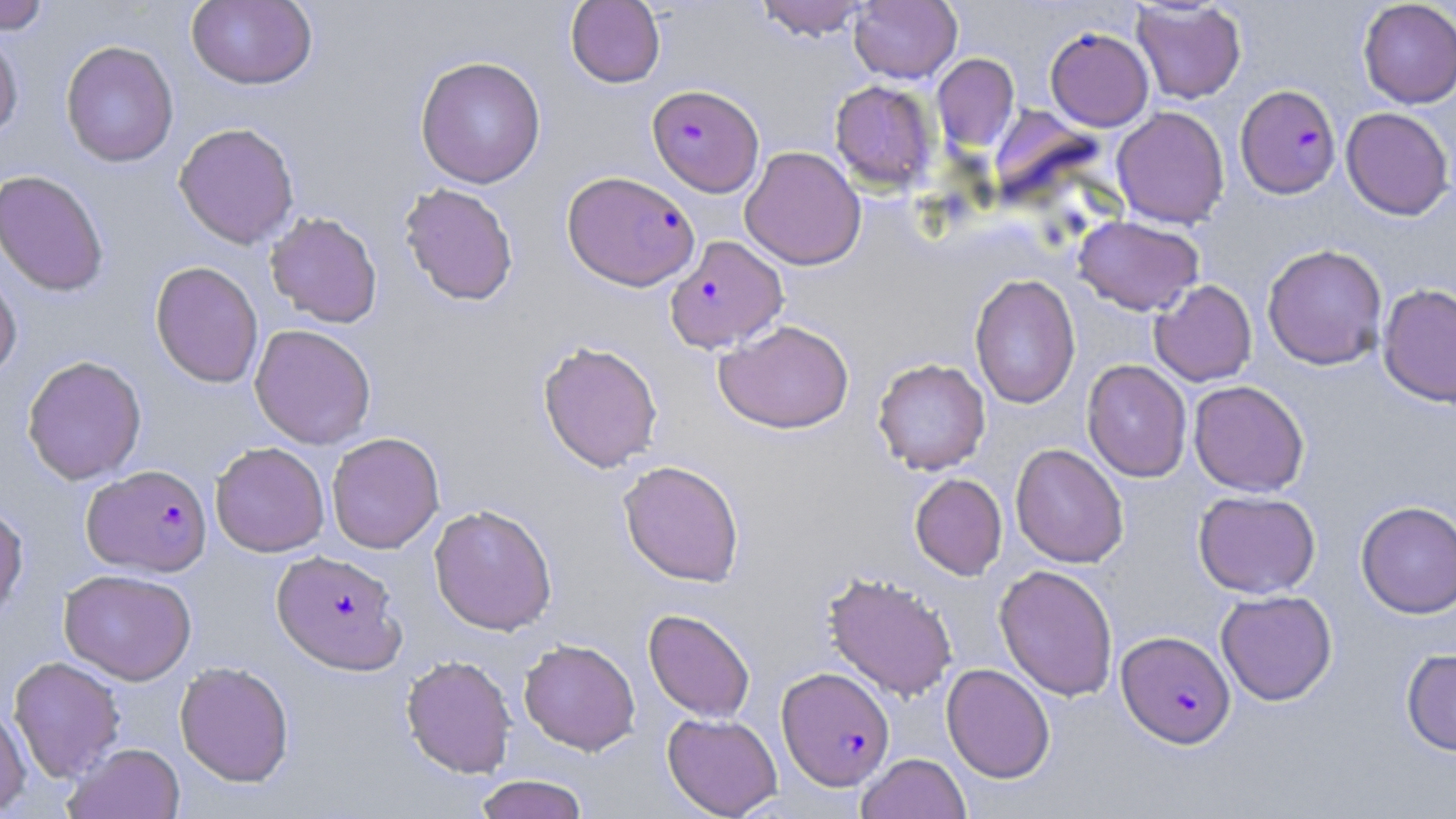
Summary:
  - Coordinate format: approximate bounding boxes as (x1, y1, x2, y2) in pixels
  - Plasmodium falciparum-infected red blood cell locations: (647, 84, 764, 197), (1236, 84, 1341, 199), (562, 170, 700, 291), (665, 235, 788, 354), (83, 464, 212, 577), (272, 550, 406, 675), (1117, 630, 1235, 748), (777, 666, 894, 790)
  - Uninfected red blood cell locations: (0, 0, 52, 33), (186, 0, 317, 90), (565, 0, 665, 87), (752, 0, 872, 40), (849, 0, 962, 83), (1131, 1, 1247, 104), (1358, 1, 1456, 108), (1045, 26, 1154, 131), (0, 27, 23, 144), (60, 40, 179, 167), (932, 53, 1020, 152), (415, 55, 546, 188), (829, 80, 938, 191), (991, 105, 1106, 212), (1111, 106, 1230, 229), (1341, 107, 1455, 220), (174, 122, 299, 249), (740, 146, 866, 270), (0, 169, 110, 296), (399, 182, 519, 306), (265, 211, 383, 328), (1073, 216, 1204, 315), (1262, 243, 1388, 370), (150, 261, 264, 388), (0, 264, 22, 382), (969, 273, 1081, 409), (1150, 280, 1257, 386), (1377, 283, 1456, 408), (714, 319, 854, 433), (250, 324, 376, 449), (538, 340, 664, 473), (22, 355, 147, 485), (872, 357, 991, 475), (1081, 360, 1192, 482), (1188, 380, 1310, 497), (326, 431, 445, 554), (210, 442, 329, 557), (1010, 443, 1129, 568), (618, 459, 745, 586), (909, 474, 1007, 580), (1193, 490, 1320, 598), (0, 501, 28, 624), (1356, 501, 1456, 618), (428, 504, 558, 635), (994, 564, 1118, 701), (59, 568, 197, 685), (822, 570, 958, 701), (1216, 590, 1337, 705), (643, 609, 756, 722), (518, 638, 640, 755), (1401, 648, 1456, 756), (401, 654, 516, 778), (8, 656, 125, 782), (175, 661, 294, 786), (941, 663, 1055, 783), (0, 702, 31, 817), (662, 712, 782, 818), (66, 742, 185, 819), (857, 752, 971, 819), (474, 774, 589, 819)
  - Slide-level diagnosis: Plasmodium falciparum
  - Modality: optical microscopy
  - Field of view: single
  - Image size: 1456×819 pixels
  - Magnification: 1000x
  - Stain: May-Grünwald-Giemsa
  - Preparation: thin blood smear